Classify this cell by malaria status.
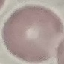

It is uninfected.

{
  "capture": "smartphone through the microscope eyepiece",
  "stain": "Giemsa",
  "preparation": "thin blood film",
  "image_type": "cell patch, automatically extracted from a larger field of view and resized to 64 × 64 pixels"
}